Point out each Plasmodium parasite.
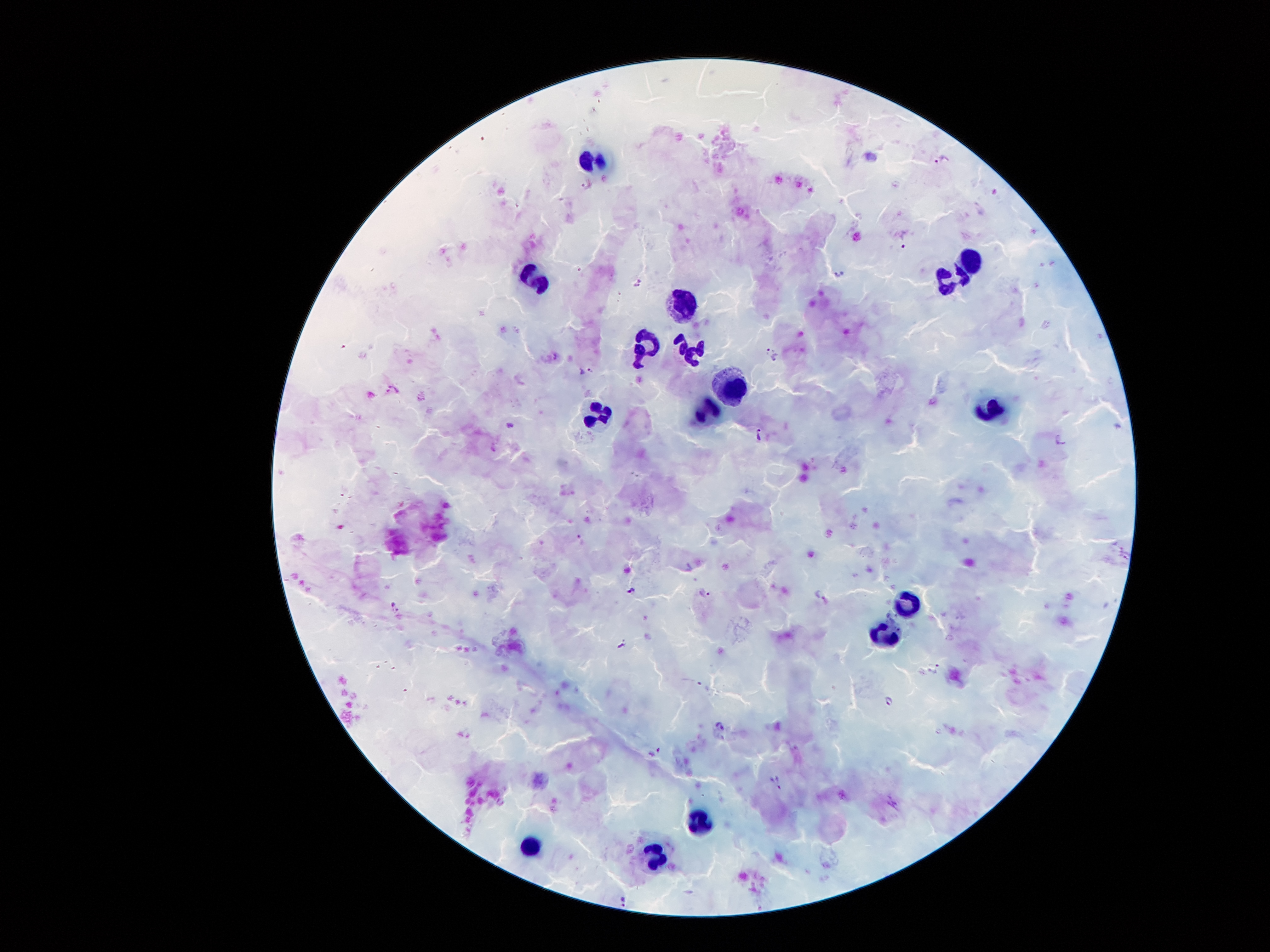

Approximate centers as {x, y} in pixels.
Plasmodium parasites: {941, 160}, {589, 371}, {510, 425}, {760, 435}, {1061, 440}, {583, 540}, {633, 588}, {705, 594}, {820, 595}, {396, 608}, {891, 701}, {721, 726}, {655, 754}, {777, 782}, {622, 901}.

leukocyte locations = {595, 162}, {974, 261}, {943, 279}, {537, 283}, {683, 299}, {648, 345}, {687, 350}, {734, 387}, {996, 402}, {712, 409}, {601, 411}, {908, 604}, {888, 632}, {703, 820}, {530, 847}, {656, 853}
patient malaria status = infected with Plasmodium falciparum
image size = 1270×952 pixels
magnification = 100x
field of view = single
preparation = thick blood film
stain = Giemsa
capture = smartphone camera through the microscope eyepiece